Locate platelets.
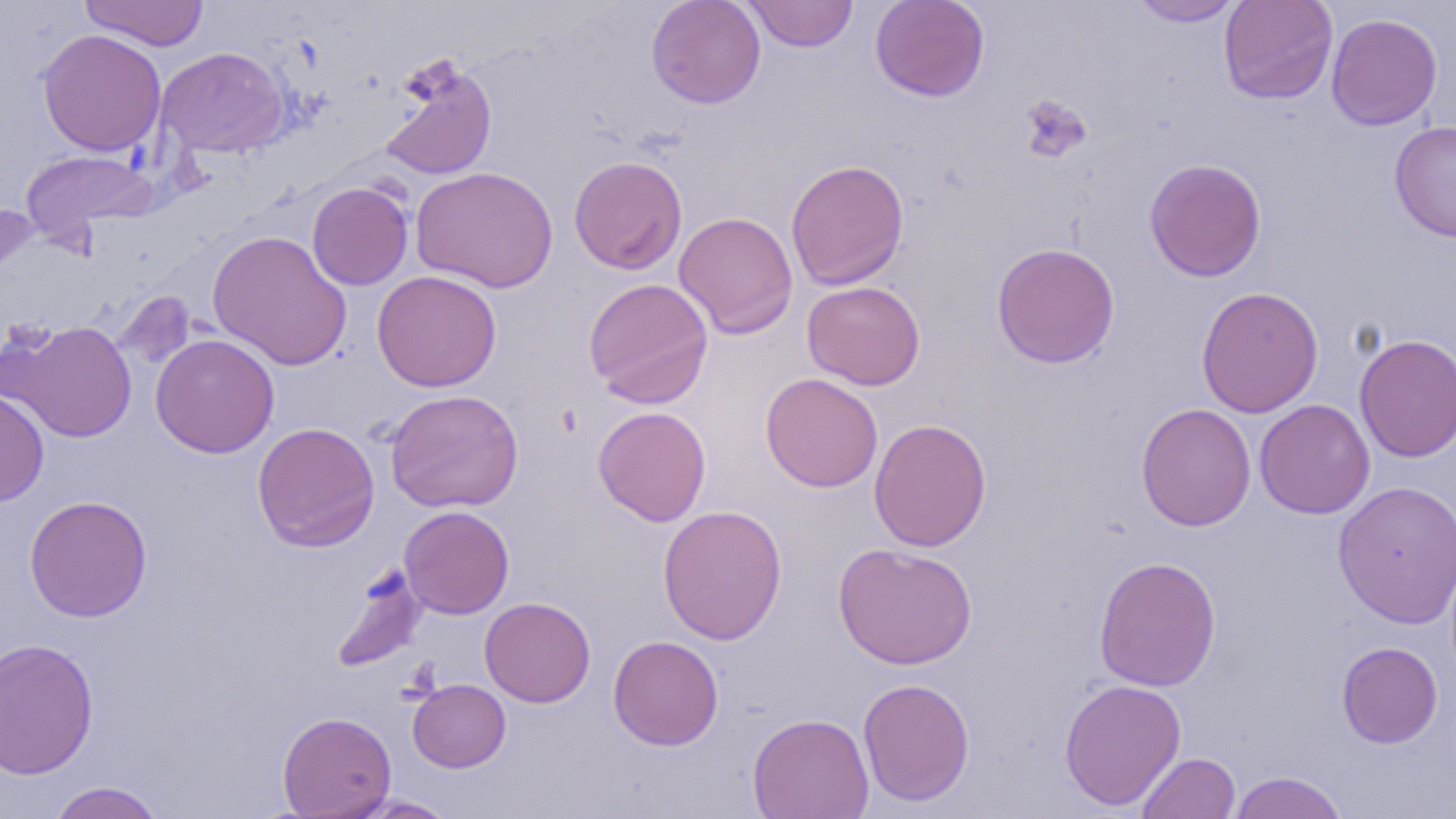

Approximate bounding boxes as (x1, y1, x2, y2) in pixels.
Platelets: (1018, 94, 1093, 164).

slide-level diagnosis = no evidence of blood parasites
magnification = 1000x
modality = optical microscopy
preparation = thin blood film
uninfected red blood cell locations = approximate bounding boxes as (x1, y1, x2, y2) in pixels: (646, 0, 766, 109), (870, 0, 990, 102), (1128, 0, 1246, 26), (1218, 0, 1338, 104), (79, 1, 209, 50), (744, 1, 858, 52), (1326, 12, 1443, 131), (37, 29, 166, 157), (156, 46, 289, 158), (377, 54, 498, 183), (1389, 119, 1456, 242), (20, 148, 158, 245), (568, 155, 688, 275), (1144, 158, 1267, 282), (785, 159, 909, 291), (410, 166, 559, 293), (306, 182, 413, 291), (0, 197, 38, 318), (673, 210, 799, 339), (208, 230, 352, 371), (992, 242, 1120, 368), (371, 270, 502, 392), (583, 277, 714, 408), (802, 281, 925, 390), (1196, 286, 1324, 418), (111, 291, 196, 371), (2, 320, 138, 443), (1353, 333, 1456, 462), (151, 334, 280, 458), (760, 373, 883, 492), (0, 387, 49, 505), (384, 389, 523, 513), (1254, 399, 1375, 519), (1136, 403, 1256, 531), (592, 406, 712, 526), (868, 418, 992, 552), (252, 422, 380, 551), (1333, 479, 1456, 628), (24, 495, 152, 621), (399, 505, 514, 619), (657, 505, 787, 645), (833, 542, 977, 670), (1093, 555, 1222, 692), (330, 563, 428, 674), (479, 597, 595, 708), (608, 634, 724, 750), (0, 637, 99, 779), (1336, 641, 1443, 748), (858, 678, 975, 806), (1059, 678, 1186, 811), (407, 679, 511, 772), (278, 711, 396, 818), (747, 712, 875, 819), (1136, 752, 1241, 819), (1228, 771, 1348, 818), (47, 781, 166, 819), (352, 796, 459, 818)
image size = 1456×819 pixels
field of view = single